Assess the morphology of the red blood cells.
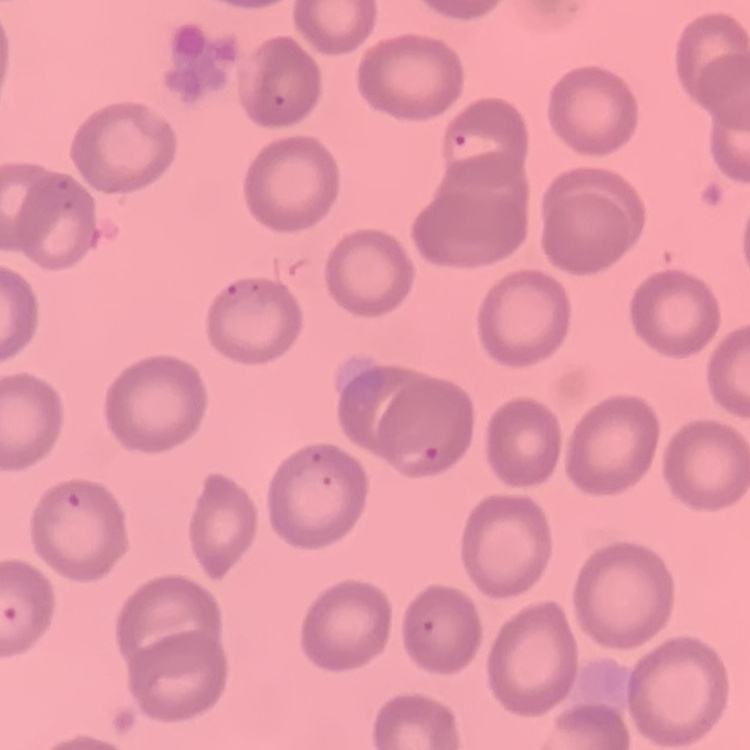
No rouleaux formation.

preparation = thin blood smear
image type = one tile cut from a larger photomicrograph
stain = Field's or Giemsa